Name the cell type shown.
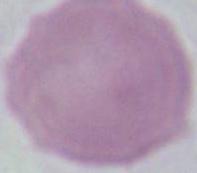
This is an erythrocyte.

magnification = 1000x
modality = micrograph